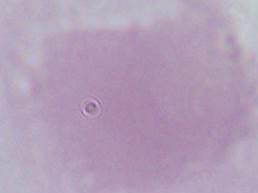

identification: red blood cell
magnification: 1000x
modality: micrograph